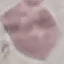

Result: no malaria parasites seen. Giemsa-stained preparation. Thin blood film. Cell patch, automatically extracted from a larger field of view and resized to 64 × 64 pixels. Photographed with a smartphone camera at the microscope eyepiece.